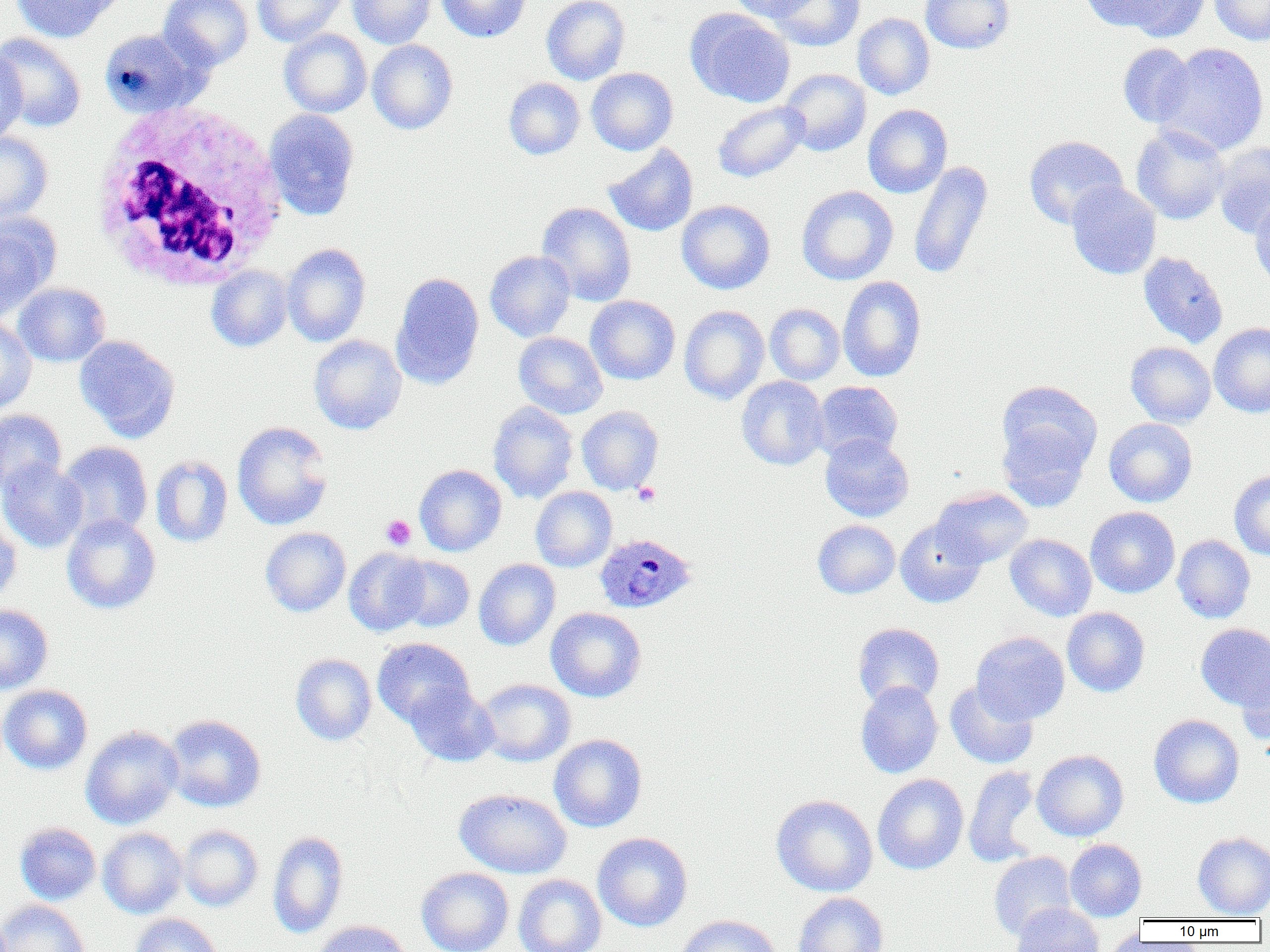
Approximate bounding boxes as named x1/y1/x2/y2 corners in pixels. Platelet locations: (x1=633, y1=482, x2=660, y2=506), (x1=380, y1=515, x2=416, y2=550). Plasmodium ovale-infected red blood cell locations: (x1=595, y1=533, x2=696, y2=614). Uninfected red blood cell locations: (x1=11, y1=0, x2=120, y2=43), (x1=158, y1=0, x2=254, y2=71), (x1=252, y1=0, x2=349, y2=46), (x1=347, y1=0, x2=436, y2=48), (x1=436, y1=0, x2=531, y2=42), (x1=541, y1=0, x2=630, y2=85), (x1=726, y1=0, x2=816, y2=21), (x1=768, y1=0, x2=864, y2=51), (x1=920, y1=0, x2=1015, y2=54), (x1=1079, y1=0, x2=1170, y2=32), (x1=1098, y1=0, x2=1212, y2=41), (x1=1209, y1=0, x2=1270, y2=46), (x1=685, y1=9, x2=795, y2=108), (x1=852, y1=13, x2=934, y2=100), (x1=98, y1=28, x2=211, y2=118), (x1=279, y1=29, x2=372, y2=118), (x1=0, y1=32, x2=87, y2=132), (x1=367, y1=40, x2=458, y2=134), (x1=1155, y1=42, x2=1269, y2=156), (x1=1118, y1=43, x2=1196, y2=127), (x1=0, y1=48, x2=28, y2=144), (x1=586, y1=67, x2=678, y2=155), (x1=780, y1=68, x2=871, y2=156), (x1=504, y1=77, x2=584, y2=159), (x1=712, y1=100, x2=810, y2=183), (x1=863, y1=104, x2=952, y2=198), (x1=263, y1=109, x2=360, y2=220), (x1=1131, y1=125, x2=1230, y2=224), (x1=0, y1=131, x2=53, y2=225), (x1=1024, y1=135, x2=1128, y2=229), (x1=1212, y1=142, x2=1270, y2=239), (x1=602, y1=143, x2=699, y2=237), (x1=908, y1=161, x2=993, y2=280), (x1=1066, y1=181, x2=1161, y2=279), (x1=797, y1=186, x2=898, y2=285), (x1=1249, y1=196, x2=1270, y2=290), (x1=676, y1=199, x2=776, y2=294), (x1=536, y1=202, x2=637, y2=306), (x1=0, y1=215, x2=59, y2=321), (x1=281, y1=243, x2=371, y2=346), (x1=485, y1=250, x2=576, y2=342), (x1=1138, y1=252, x2=1228, y2=348), (x1=206, y1=265, x2=293, y2=351), (x1=390, y1=272, x2=485, y2=389), (x1=838, y1=276, x2=927, y2=382), (x1=12, y1=282, x2=110, y2=367), (x1=585, y1=295, x2=680, y2=385), (x1=765, y1=303, x2=845, y2=385), (x1=679, y1=305, x2=769, y2=404), (x1=0, y1=317, x2=37, y2=414), (x1=1209, y1=322, x2=1270, y2=418), (x1=513, y1=332, x2=608, y2=419), (x1=308, y1=334, x2=407, y2=434), (x1=75, y1=335, x2=180, y2=441), (x1=1125, y1=341, x2=1216, y2=427), (x1=736, y1=376, x2=829, y2=470), (x1=812, y1=381, x2=903, y2=461), (x1=997, y1=381, x2=1102, y2=476), (x1=488, y1=401, x2=579, y2=503), (x1=577, y1=406, x2=663, y2=495), (x1=0, y1=409, x2=66, y2=496), (x1=1104, y1=418, x2=1198, y2=507), (x1=232, y1=421, x2=334, y2=530), (x1=997, y1=422, x2=1092, y2=513), (x1=820, y1=433, x2=914, y2=522), (x1=57, y1=441, x2=153, y2=540), (x1=150, y1=455, x2=233, y2=547), (x1=0, y1=459, x2=88, y2=552), (x1=414, y1=465, x2=506, y2=556), (x1=1229, y1=470, x2=1270, y2=560), (x1=530, y1=486, x2=617, y2=572), (x1=931, y1=487, x2=1034, y2=569), (x1=1085, y1=506, x2=1180, y2=598), (x1=0, y1=514, x2=22, y2=606), (x1=61, y1=514, x2=161, y2=614), (x1=895, y1=518, x2=986, y2=608), (x1=812, y1=519, x2=900, y2=599), (x1=260, y1=527, x2=351, y2=617), (x1=1005, y1=533, x2=1097, y2=621), (x1=1172, y1=534, x2=1255, y2=624), (x1=344, y1=547, x2=430, y2=636), (x1=392, y1=555, x2=474, y2=632), (x1=474, y1=559, x2=560, y2=650), (x1=0, y1=605, x2=53, y2=694), (x1=545, y1=607, x2=646, y2=702), (x1=1062, y1=607, x2=1150, y2=697), (x1=852, y1=623, x2=945, y2=708), (x1=1196, y1=623, x2=1270, y2=710), (x1=971, y1=631, x2=1069, y2=725), (x1=372, y1=637, x2=475, y2=727), (x1=290, y1=653, x2=377, y2=746), (x1=1237, y1=659, x2=1270, y2=748), (x1=476, y1=678, x2=576, y2=767), (x1=945, y1=679, x2=1039, y2=769), (x1=855, y1=681, x2=943, y2=778), (x1=405, y1=683, x2=499, y2=767), (x1=0, y1=684, x2=93, y2=775), (x1=163, y1=714, x2=266, y2=812), (x1=1148, y1=714, x2=1244, y2=808), (x1=80, y1=725, x2=183, y2=830), (x1=549, y1=733, x2=647, y2=832), (x1=1032, y1=749, x2=1129, y2=841), (x1=963, y1=765, x2=1042, y2=867), (x1=872, y1=774, x2=969, y2=875), (x1=454, y1=788, x2=572, y2=879), (x1=771, y1=794, x2=878, y2=897), (x1=15, y1=822, x2=101, y2=905), (x1=178, y1=825, x2=263, y2=911), (x1=98, y1=827, x2=187, y2=918), (x1=267, y1=831, x2=348, y2=938), (x1=592, y1=832, x2=693, y2=932), (x1=1192, y1=832, x2=1270, y2=918), (x1=1065, y1=839, x2=1146, y2=921), (x1=988, y1=851, x2=1077, y2=942), (x1=416, y1=867, x2=514, y2=952), (x1=513, y1=874, x2=606, y2=952), (x1=793, y1=892, x2=888, y2=952), (x1=0, y1=899, x2=90, y2=952), (x1=1010, y1=902, x2=1105, y2=952), (x1=130, y1=913, x2=223, y2=952), (x1=673, y1=914, x2=782, y2=952), (x1=312, y1=920, x2=411, y2=952), (x1=1105, y1=925, x2=1142, y2=952). White blood cell locations: (x1=88, y1=101, x2=287, y2=292). Slide-level diagnosis: Plasmodium ovale. Single field of view. 1000x magnification. Thin blood smear. Light microscopy. Image is 1270×952 pixels.